Classify this cell by malaria status.
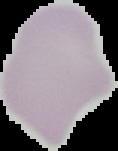
Uninfected.

image type = segmented cell region on a black background
image size = 118×151 pixels
preparation = thin blood film